Assess the morphology of the red blood cells.
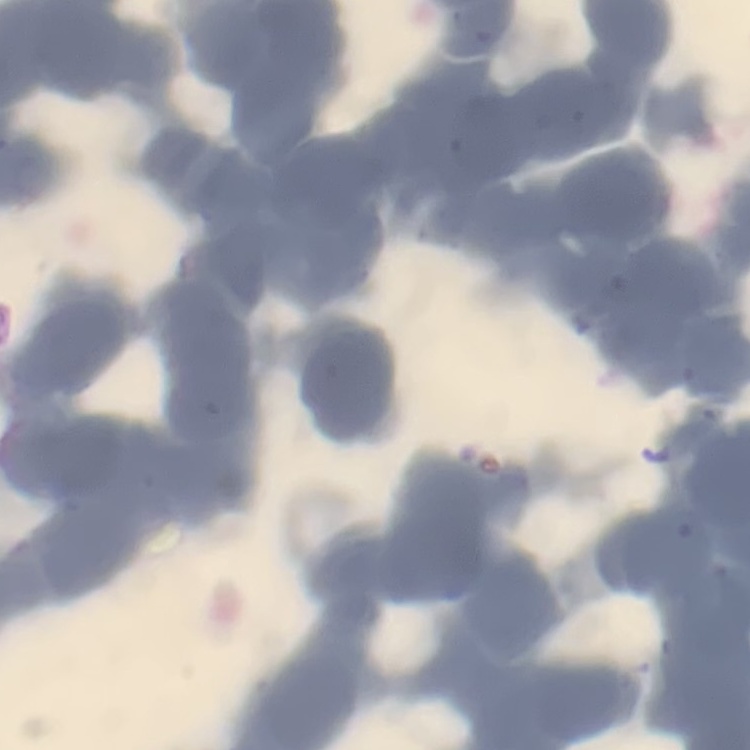

Rouleaux formation.

{
  "image_type": "one tile cut from a larger photomicrograph",
  "stain": "Field's or Giemsa",
  "preparation": "thin peripheral smear"
}